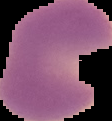
result = malaria parasites detected
image size = 112×121 pixels
preparation = thin blood film
image type = segmented cell region on a black background